Report the malaria status of this cell.
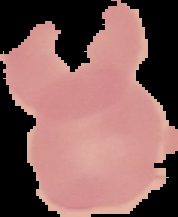
It is uninfected.

image_size: 178×217 pixels
preparation: thin blood smear
image_type: cell region segmented out of the field of view; surrounding area masked to black